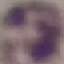
Summary:
  - Malaria status: uninfected
  - Capture: smartphone camera at the microscope eyepiece
  - Stain: Giemsa
  - Image type: cell patch, automatically extracted from a larger field of view and resized to 64 × 64 pixels
  - Preparation: thin blood smear